Locate every malaria parasite and every leukocyte.
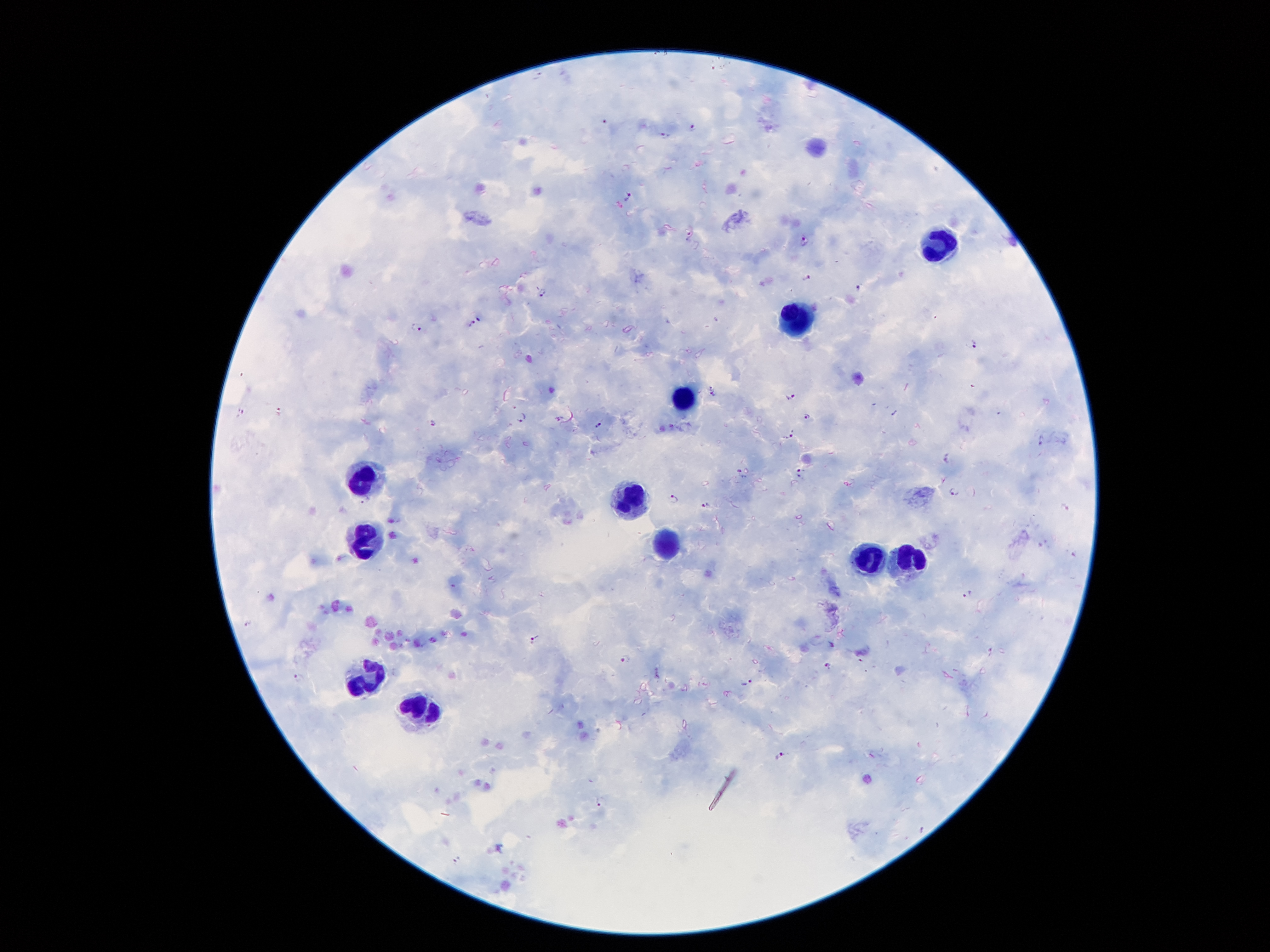
Approximate centers as [x, y] in pixels.
Malaria parasites: [604, 120], [694, 127], [665, 135], [628, 197], [690, 234], [803, 239], [809, 277], [857, 287], [542, 292], [480, 317], [471, 323], [416, 327], [972, 345], [714, 394], [791, 396], [242, 412], [807, 416], [522, 417], [558, 418], [433, 422], [598, 425], [790, 434], [1039, 438], [947, 459], [799, 468], [740, 471], [801, 477], [953, 490], [674, 499], [705, 505], [1066, 508], [966, 594], [247, 623], [535, 640], [626, 659], [827, 665], [299, 676], [748, 683], [779, 755], [598, 800], [458, 858].
Leukocytes: [943, 244], [793, 317], [685, 396], [363, 476], [630, 494], [373, 536], [663, 542], [866, 556], [907, 557], [367, 675], [422, 708].

preparation: thick blood film
stain: Giemsa
image_size: 1270×952 pixels
capture: smartphone through the microscope eyepiece
magnification: 100x
patient_malaria_status: infected with Plasmodium falciparum
field_of_view: one from this slide